Outline each blood parasite and name the species.
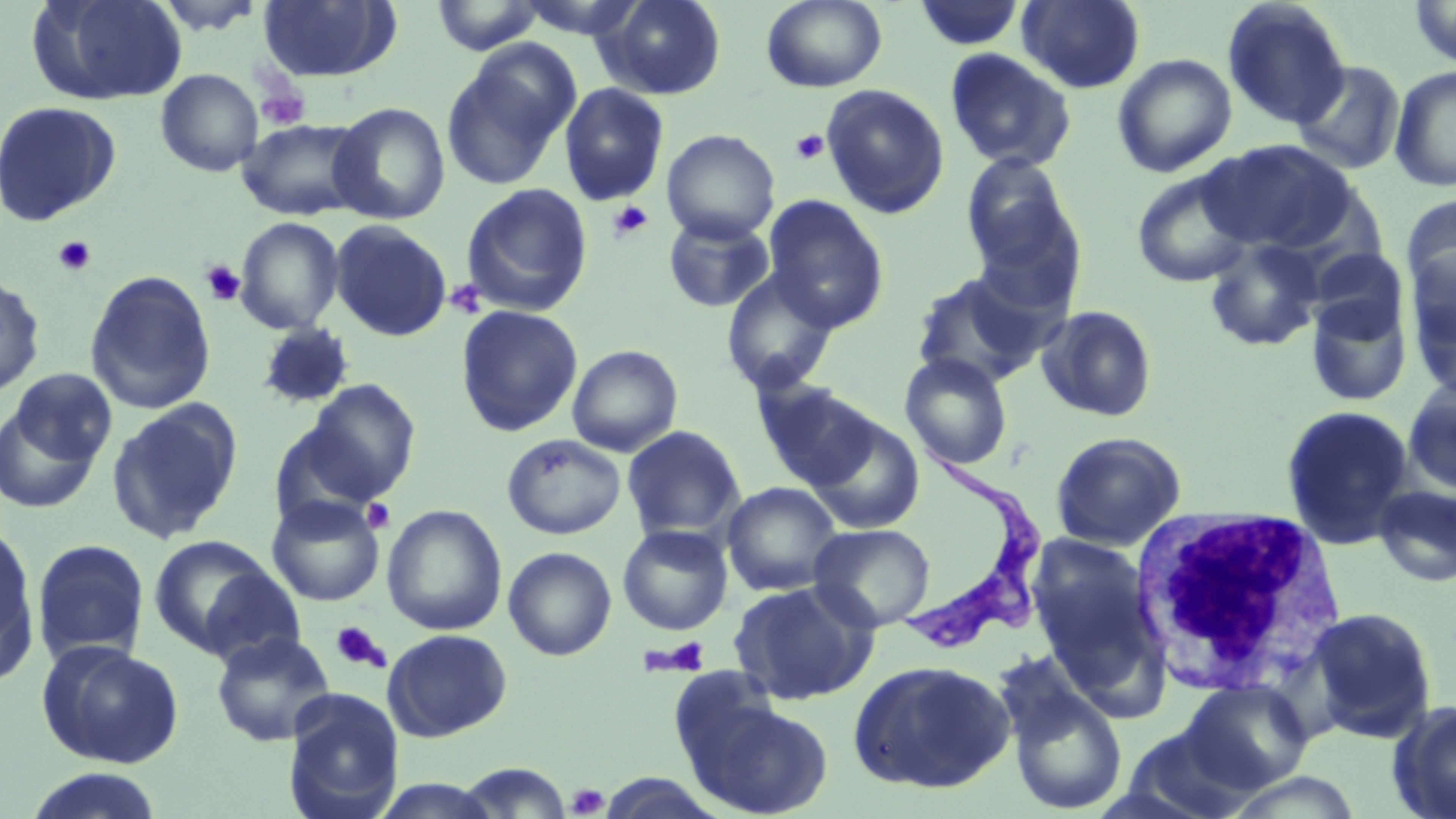

Approximate bounding boxes as named x1/y1/x2/y2 corners in pixels.
Trypanosoma brucei: (x1=895, y1=437, x2=1040, y2=650).
No Plasmodium falciparum, Plasmodium ovale, Plasmodium malariae, Plasmodium vivax, or Babesia divergens observed.

{
  "slide_level_diagnosis": "Trypanosoma brucei",
  "white_blood_cell_locations": "approximate bounding boxes as named x1/y1/x2/y2 corners in pixels: (x1=1129, y1=506, x2=1353, y2=697)",
  "platelet_locations": "approximate bounding boxes as named x1/y1/x2/y2 corners in pixels: (x1=253, y1=77, x2=309, y2=131), (x1=791, y1=130, x2=830, y2=165), (x1=607, y1=200, x2=653, y2=242), (x1=53, y1=236, x2=95, y2=277), (x1=200, y1=259, x2=246, y2=307), (x1=446, y1=279, x2=488, y2=319), (x1=361, y1=498, x2=395, y2=534), (x1=330, y1=621, x2=389, y2=672), (x1=648, y1=636, x2=711, y2=676), (x1=567, y1=784, x2=609, y2=817)",
  "field_of_view": "one of a larger specimen",
  "modality": "optical microscopy",
  "preparation": "thin blood smear",
  "magnification": "1000x",
  "stain": "May-Grünwald-Giemsa",
  "image_size": "1456×819 pixels",
  "uninfected_red_blood_cell_locations": "approximate bounding boxes as named x1/y1/x2/y2 corners in pixels: (x1=28, y1=0, x2=186, y2=106), (x1=149, y1=0, x2=270, y2=36), (x1=429, y1=0, x2=547, y2=56), (x1=511, y1=0, x2=650, y2=40), (x1=594, y1=0, x2=727, y2=100), (x1=761, y1=0, x2=887, y2=92), (x1=1017, y1=0, x2=1145, y2=93), (x1=1222, y1=0, x2=1351, y2=129), (x1=1410, y1=0, x2=1455, y2=67), (x1=257, y1=1, x2=402, y2=83), (x1=913, y1=1, x2=1026, y2=51), (x1=440, y1=45, x2=579, y2=191), (x1=944, y1=48, x2=1077, y2=172), (x1=1113, y1=53, x2=1237, y2=177), (x1=1292, y1=60, x2=1406, y2=175), (x1=1389, y1=65, x2=1456, y2=192), (x1=155, y1=70, x2=262, y2=176), (x1=558, y1=82, x2=670, y2=206), (x1=820, y1=83, x2=950, y2=219), (x1=0, y1=101, x2=122, y2=227), (x1=328, y1=102, x2=450, y2=225), (x1=236, y1=119, x2=369, y2=221), (x1=662, y1=129, x2=780, y2=244), (x1=1200, y1=139, x2=1358, y2=255), (x1=959, y1=152, x2=1081, y2=284), (x1=1131, y1=168, x2=1258, y2=288), (x1=460, y1=182, x2=594, y2=317), (x1=1401, y1=194, x2=1456, y2=306), (x1=762, y1=195, x2=889, y2=332), (x1=663, y1=213, x2=776, y2=312), (x1=235, y1=216, x2=344, y2=334), (x1=329, y1=220, x2=452, y2=342), (x1=1202, y1=237, x2=1328, y2=353), (x1=1305, y1=247, x2=1409, y2=344), (x1=1406, y1=253, x2=1456, y2=391), (x1=721, y1=267, x2=841, y2=394), (x1=909, y1=269, x2=1051, y2=389), (x1=84, y1=270, x2=216, y2=415), (x1=0, y1=271, x2=45, y2=399), (x1=1304, y1=295, x2=1413, y2=408), (x1=1036, y1=304, x2=1159, y2=423), (x1=456, y1=305, x2=583, y2=437), (x1=255, y1=323, x2=356, y2=410), (x1=566, y1=344, x2=684, y2=457), (x1=899, y1=353, x2=1013, y2=470), (x1=8, y1=367, x2=118, y2=468), (x1=1403, y1=375, x2=1456, y2=499), (x1=750, y1=377, x2=879, y2=491), (x1=298, y1=378, x2=421, y2=506), (x1=0, y1=401, x2=106, y2=514), (x1=106, y1=401, x2=243, y2=544), (x1=1280, y1=404, x2=1415, y2=548), (x1=804, y1=414, x2=925, y2=534), (x1=622, y1=425, x2=745, y2=542), (x1=1050, y1=431, x2=1186, y2=551), (x1=501, y1=433, x2=626, y2=540), (x1=721, y1=481, x2=844, y2=596), (x1=1373, y1=484, x2=1456, y2=588), (x1=266, y1=494, x2=386, y2=607), (x1=382, y1=504, x2=507, y2=636), (x1=0, y1=520, x2=40, y2=680), (x1=808, y1=523, x2=935, y2=632), (x1=617, y1=524, x2=734, y2=636), (x1=146, y1=534, x2=286, y2=661), (x1=1026, y1=534, x2=1165, y2=692), (x1=31, y1=539, x2=151, y2=667), (x1=503, y1=546, x2=617, y2=661), (x1=195, y1=564, x2=307, y2=669), (x1=728, y1=580, x2=879, y2=706), (x1=1301, y1=606, x2=1438, y2=743), (x1=383, y1=628, x2=513, y2=741), (x1=210, y1=631, x2=335, y2=746), (x1=37, y1=641, x2=185, y2=769), (x1=847, y1=659, x2=1015, y2=794), (x1=1003, y1=678, x2=1129, y2=816), (x1=1181, y1=680, x2=1312, y2=793), (x1=678, y1=688, x2=834, y2=819), (x1=282, y1=691, x2=404, y2=819), (x1=1386, y1=699, x2=1456, y2=819), (x1=1122, y1=723, x2=1259, y2=818), (x1=454, y1=762, x2=576, y2=818), (x1=23, y1=768, x2=167, y2=819), (x1=367, y1=778, x2=508, y2=818)"
}